Give the position of every Plasmodium parasite visible.
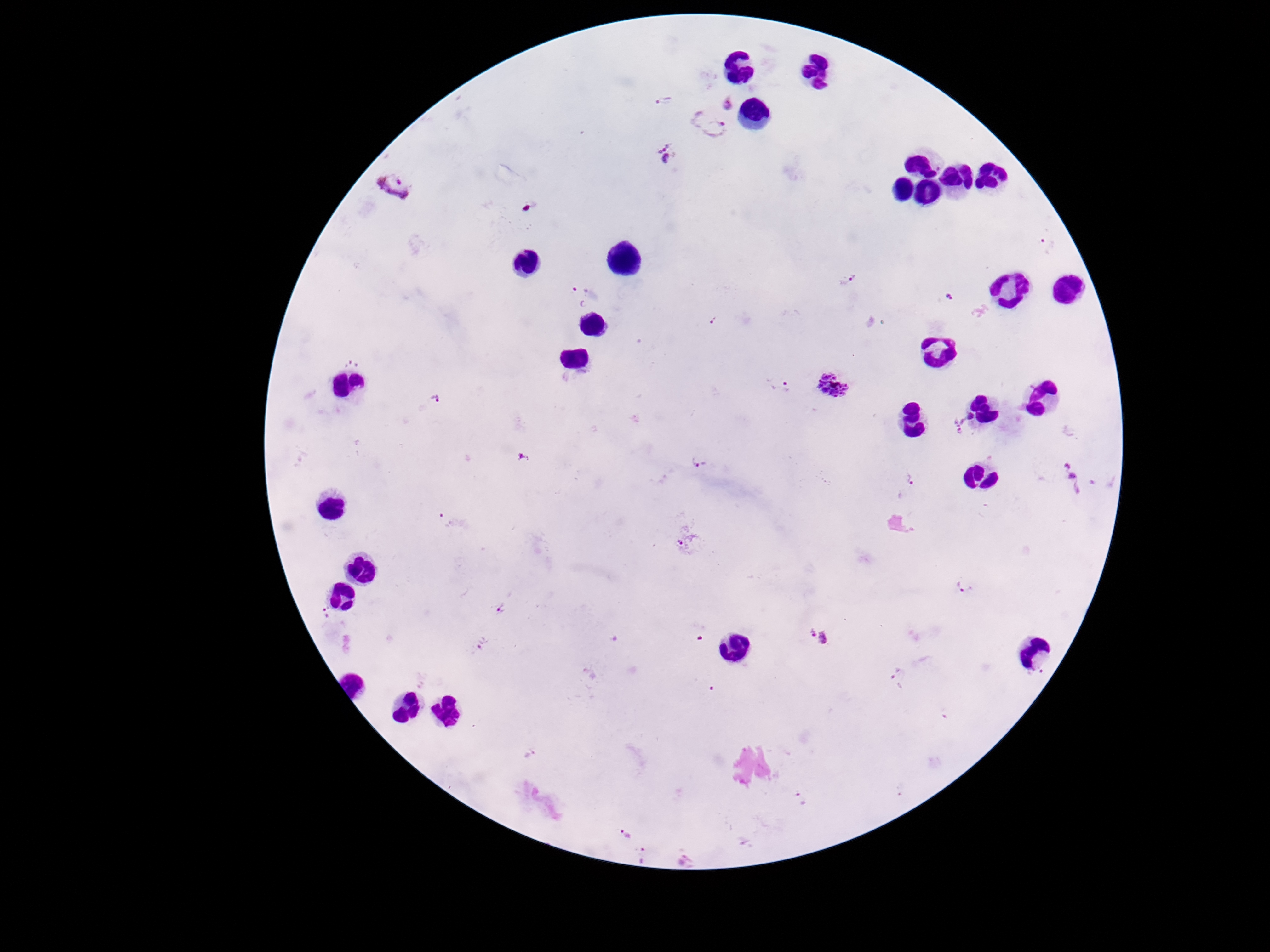

Approximate centers as {x, y} in pixels.
Plasmodium parasites: {664, 100}, {728, 105}, {708, 124}, {667, 152}, {395, 186}, {529, 206}, {1048, 244}, {848, 277}, {582, 294}, {950, 297}, {351, 364}, {779, 385}, {832, 387}, {436, 397}, {964, 424}, {524, 456}, {698, 461}, {1071, 475}, {909, 478}, {447, 520}, {963, 586}, {502, 609}, {326, 612}, {821, 637}, {483, 643}, {896, 674}, {531, 755}, {801, 799}, {626, 834}, {645, 856}, {686, 862}.

Single field of view. Patient malaria status: infected. Image is 1270×952 pixels. Giemsa-stained preparation. 100x magnification. Thick blood smear. Smartphone photograph taken through the microscope eyepiece.